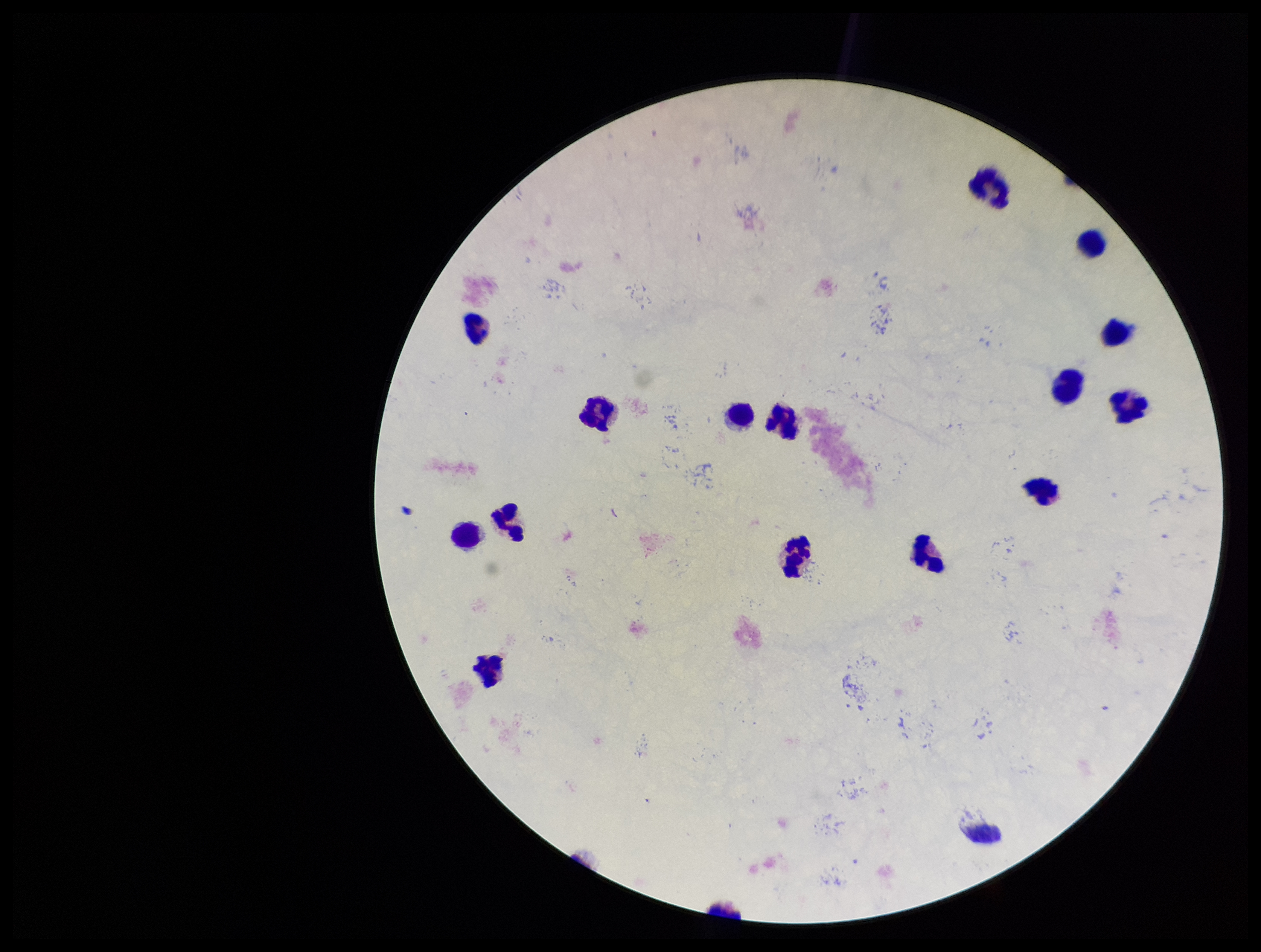

Preparation: thick blood smear. Image is 1261×952 pixels. Plasmodium parasites: none identified. Stained with Giemsa. Smartphone photograph taken through the eyepiece of a microscope. One field from this slide. Patient malaria status: negative. Leukocyte count: 15. Parasite count: 0.